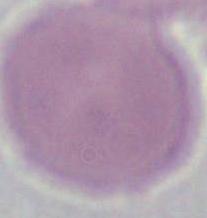 A red blood cell is seen. Micrograph. Captured at 1000x magnification.